State the blood parasite species.
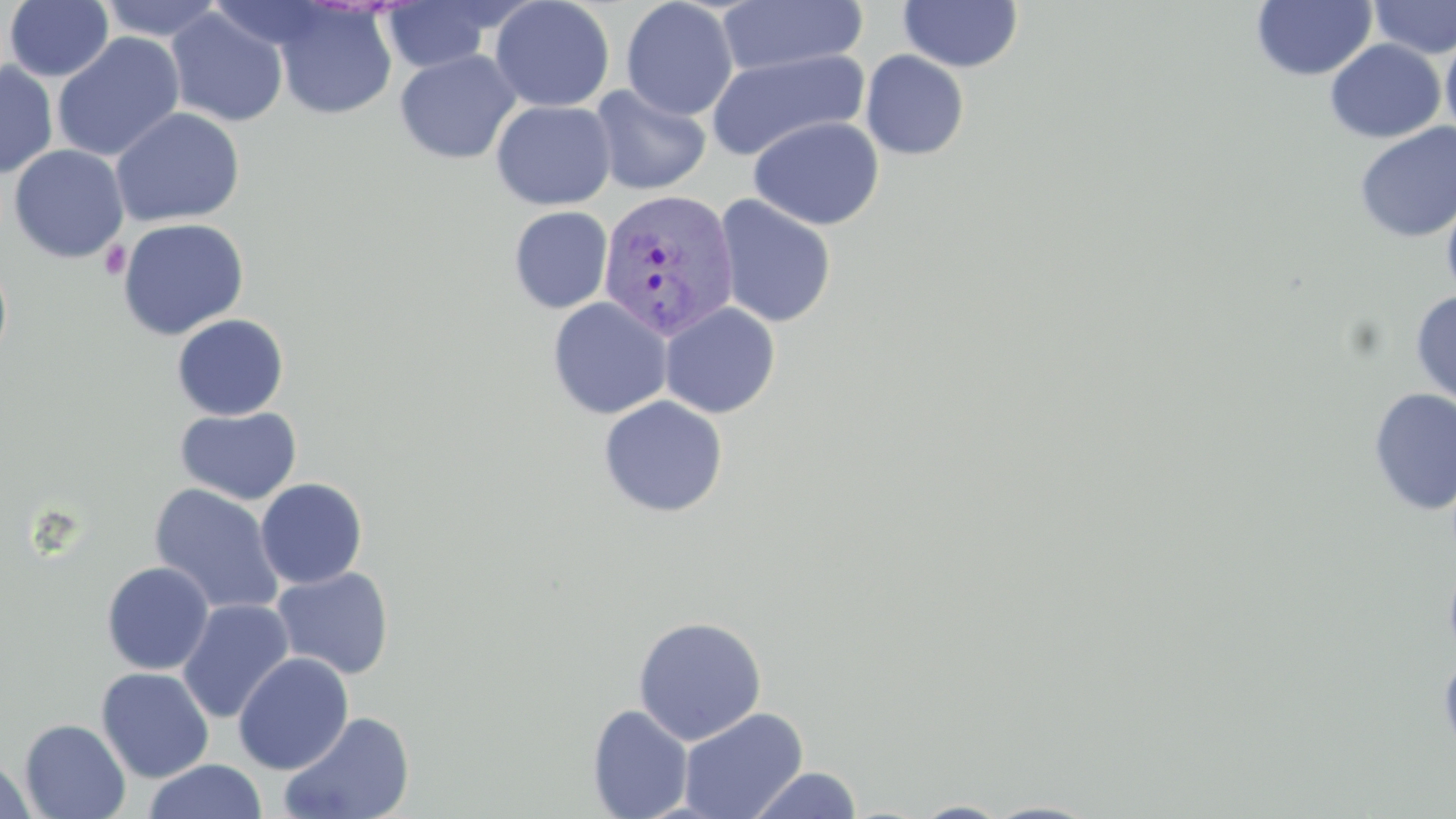
Plasmodium vivax.

{
  "stain": "May-Grünwald-Giemsa",
  "field_of_view": "single",
  "platelet_locations": "approximate bounding boxes as named x1/y1/x2/y2 corners in pixels: (x1=100, y1=241, x2=131, y2=279)",
  "magnification": "1000x",
  "plasmodium_vivax_infected_red_blood_cell_locations": "approximate bounding boxes as named x1/y1/x2/y2 corners in pixels: (x1=598, y1=188, x2=740, y2=341)",
  "preparation": "thin blood film",
  "image_size": "1456×819 pixels",
  "uninfected_red_blood_cell_locations": "approximate bounding boxes as named x1/y1/x2/y2 corners in pixels: (x1=96, y1=0, x2=227, y2=42), (x1=489, y1=0, x2=615, y2=113), (x1=620, y1=0, x2=739, y2=121), (x1=1252, y1=0, x2=1376, y2=81), (x1=1368, y1=0, x2=1456, y2=59), (x1=3, y1=1, x2=114, y2=82), (x1=380, y1=1, x2=505, y2=73), (x1=715, y1=1, x2=868, y2=78), (x1=898, y1=1, x2=1023, y2=73), (x1=273, y1=2, x2=397, y2=120), (x1=166, y1=7, x2=289, y2=127), (x1=1440, y1=28, x2=1456, y2=143), (x1=52, y1=33, x2=185, y2=162), (x1=1325, y1=39, x2=1445, y2=143), (x1=707, y1=48, x2=870, y2=161), (x1=394, y1=50, x2=522, y2=165), (x1=860, y1=50, x2=970, y2=161), (x1=0, y1=62, x2=58, y2=178), (x1=589, y1=84, x2=711, y2=196), (x1=490, y1=100, x2=616, y2=210), (x1=110, y1=107, x2=246, y2=227), (x1=749, y1=116, x2=885, y2=230), (x1=1354, y1=122, x2=1456, y2=243), (x1=8, y1=144, x2=129, y2=263), (x1=1441, y1=189, x2=1456, y2=307), (x1=714, y1=195, x2=837, y2=328), (x1=509, y1=206, x2=612, y2=313), (x1=117, y1=217, x2=250, y2=340), (x1=0, y1=254, x2=13, y2=369), (x1=1410, y1=290, x2=1456, y2=408), (x1=547, y1=297, x2=673, y2=420), (x1=659, y1=302, x2=781, y2=419), (x1=171, y1=313, x2=290, y2=421), (x1=1369, y1=388, x2=1456, y2=515), (x1=598, y1=395, x2=729, y2=518), (x1=174, y1=406, x2=302, y2=505), (x1=255, y1=478, x2=368, y2=589), (x1=148, y1=483, x2=285, y2=617), (x1=1443, y1=555, x2=1456, y2=666), (x1=101, y1=561, x2=214, y2=675), (x1=270, y1=566, x2=395, y2=680), (x1=177, y1=598, x2=294, y2=724), (x1=632, y1=615, x2=767, y2=745), (x1=1437, y1=646, x2=1456, y2=769), (x1=233, y1=652, x2=354, y2=775), (x1=96, y1=667, x2=215, y2=783), (x1=587, y1=704, x2=694, y2=819), (x1=677, y1=707, x2=809, y2=819), (x1=278, y1=711, x2=414, y2=818), (x1=19, y1=718, x2=131, y2=819), (x1=1, y1=755, x2=37, y2=819), (x1=143, y1=759, x2=268, y2=819), (x1=747, y1=766, x2=863, y2=819), (x1=982, y1=800, x2=1102, y2=818), (x1=910, y1=801, x2=1013, y2=818)",
  "modality": "light microscopy"
}